Identify the parasite.
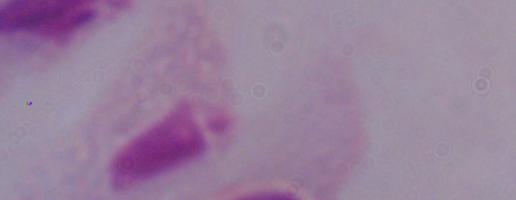
This is a trichomonad.

Summary:
  - Modality: photomicrograph
  - Magnification: 1000x